Report the malaria status of this cell.
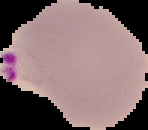
Parasitized.

image type = segmented cell region on a black background
preparation = thin blood smear
image size = 148×130 pixels